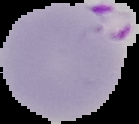

Summary:
  - Image size: 139×124 pixels
  - Malaria status: parasitized
  - Preparation: thin blood film
  - Image type: cell region segmented out of the field of view; surrounding area masked to black